Name the parasite shown.
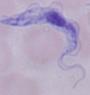
A trypanosome.

magnification = 1000x
modality = photomicrograph